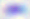

400x magnification. Toxoplasma gondii is shown. Micrograph.